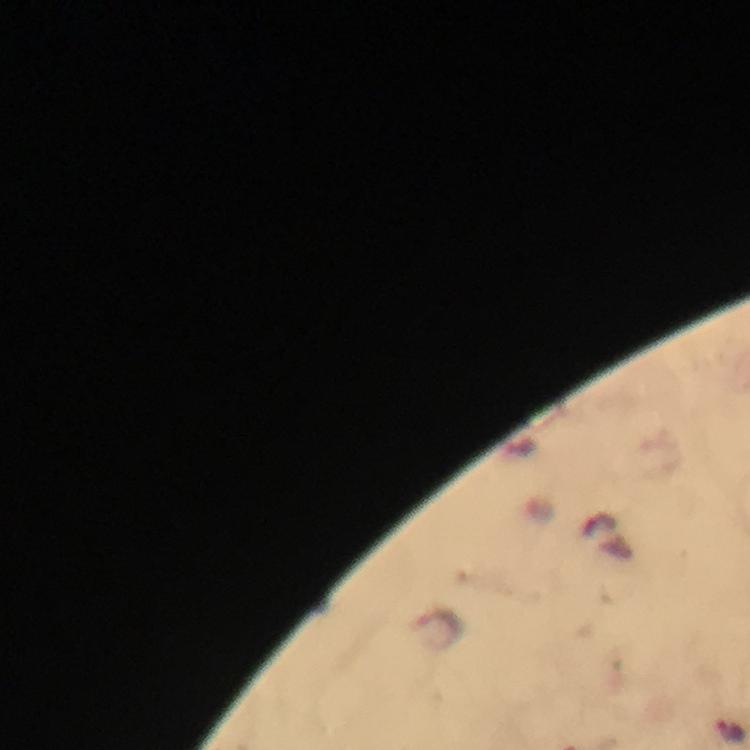

capture: smartphone photograph through a microscope
stain: Giemsa
plasmodium_parasite_locations: 'approximate object centers, in pixels from the top-left corner: (x=731, y=731)'
immersion_oil: used
preparation: thick blood film
context: from a diagnostic examination for malaria
cropped_from: a single field of view
magnification: 100x
image_size: 750×750 pixels